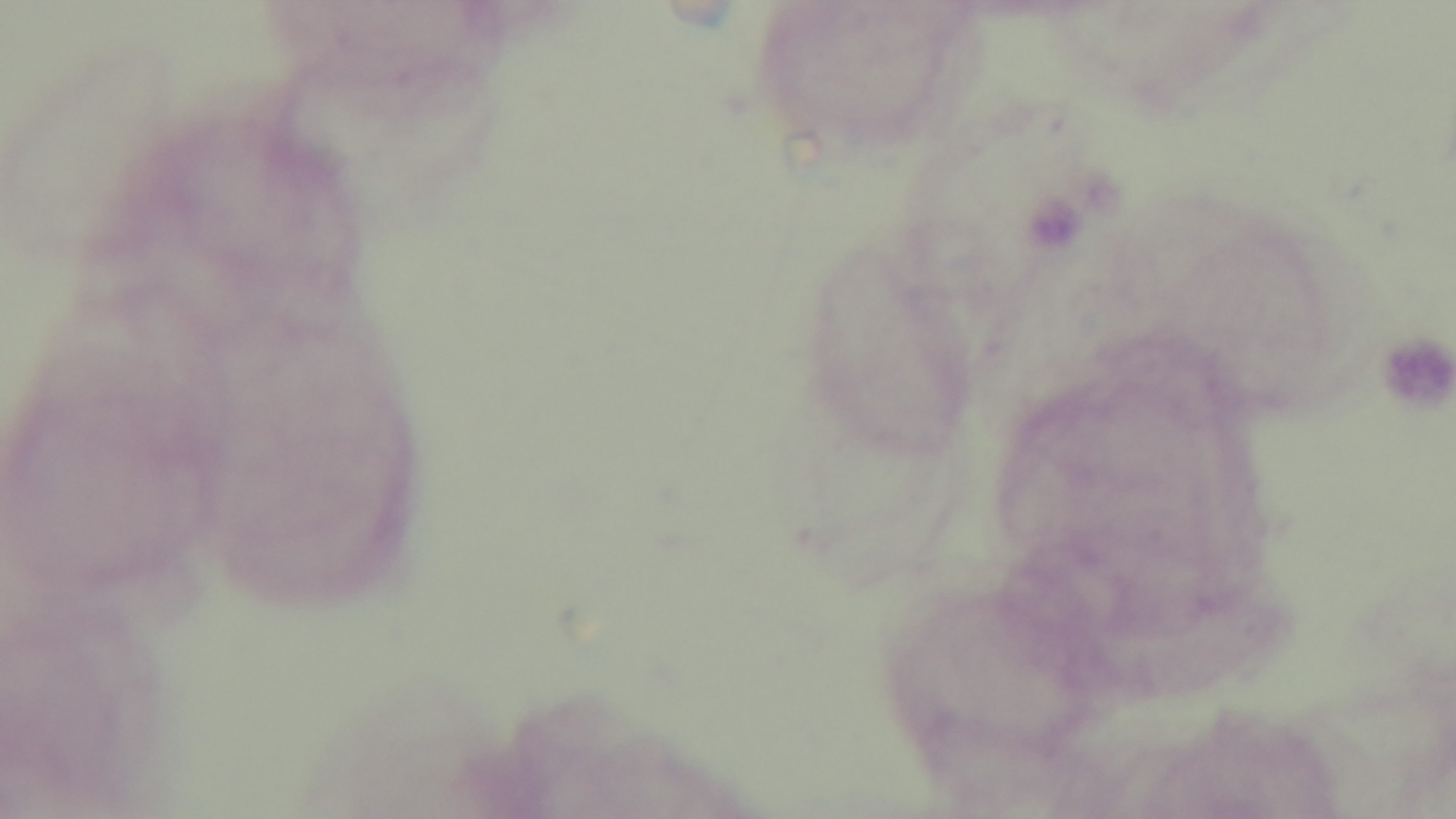
capture = mounted 4K digital camera
malaria status = negative
modality = light microscopy
stain = Giemsa
field of view = single
preparation = thick
objective = 100x oil immersion